Describe the morphology of the red blood cells.
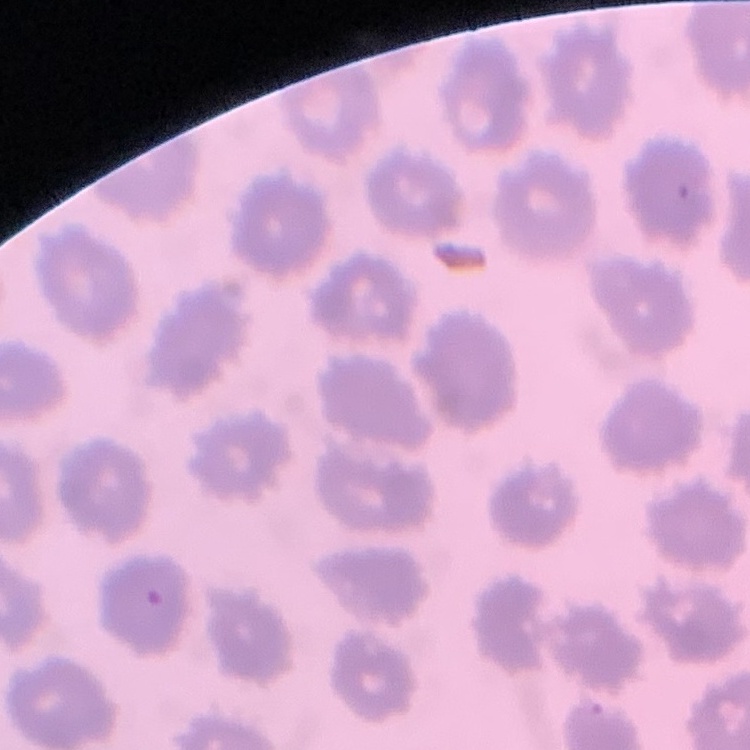
They show no rouleaux formation.

stain: Field's or Giemsa
image_type: one tile cut from a larger photomicrograph
preparation: thin blood smear